State the preparation type.
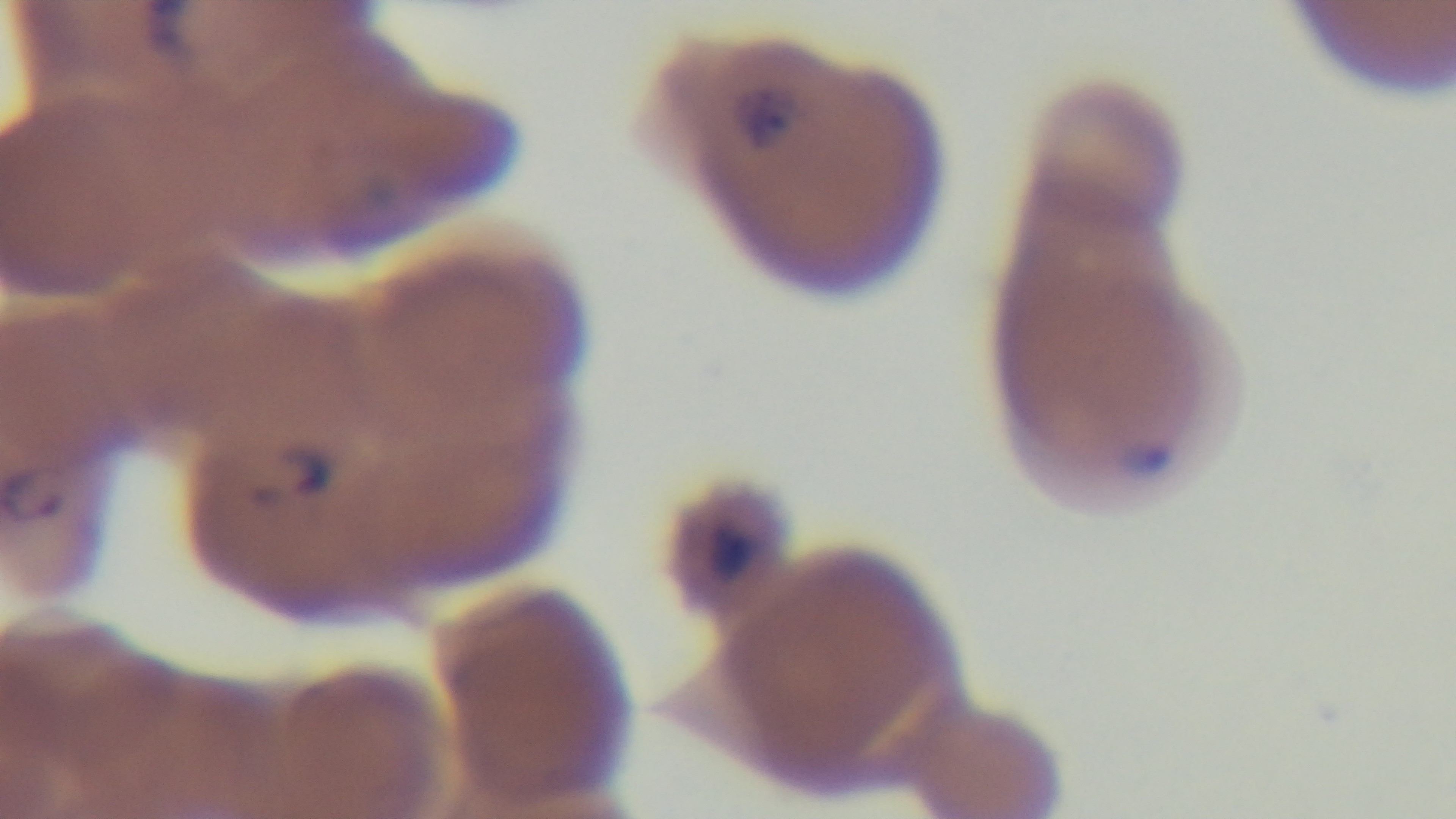
Thin.

Summary:
  - Stain: Giemsa
  - Modality: light microscopy
  - Malaria status: positive
  - Field of view: single
  - Capture: mounted 4K digital camera
  - Objective: 100x oil immersion